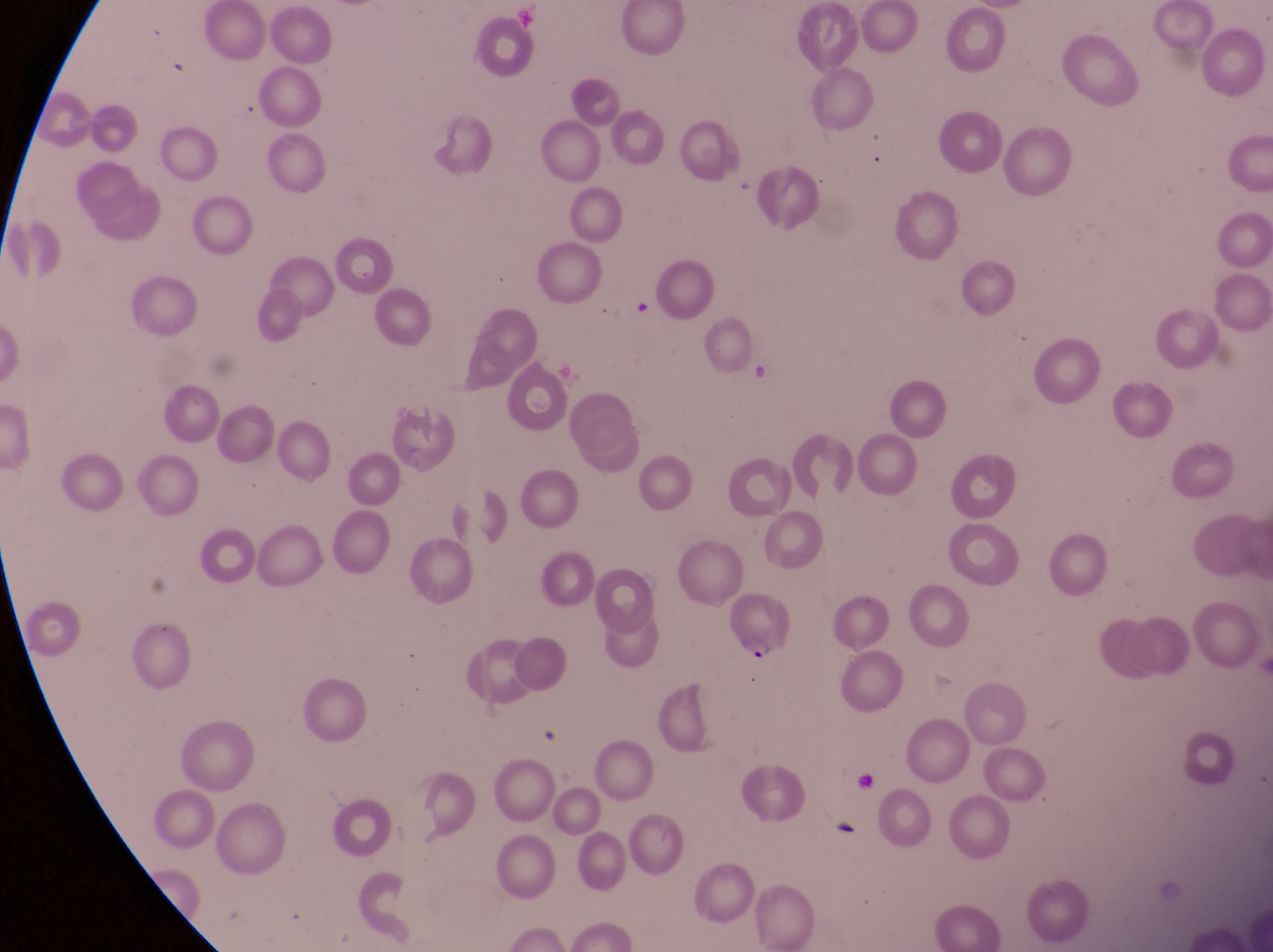
{
  "field_of_view": "single",
  "artifact_platelet_like_body_stain_precipitate_or_debris_locations": "approximate bounding boxes as (left, top, right, bottom) in pixels: (627, 289, 660, 328)",
  "magnification": "1000x",
  "capture": "smartphone photograph through the eyepiece of an Olympus CX-23 microscope",
  "country": "Uganda",
  "preparation": "thin blood smear",
  "image_size": "1273×952 pixels",
  "parasitised_red_blood_cell_locations": "approximate bounding boxes as (left, top, right, bottom) in pixels: (721, 591, 799, 671)"
}